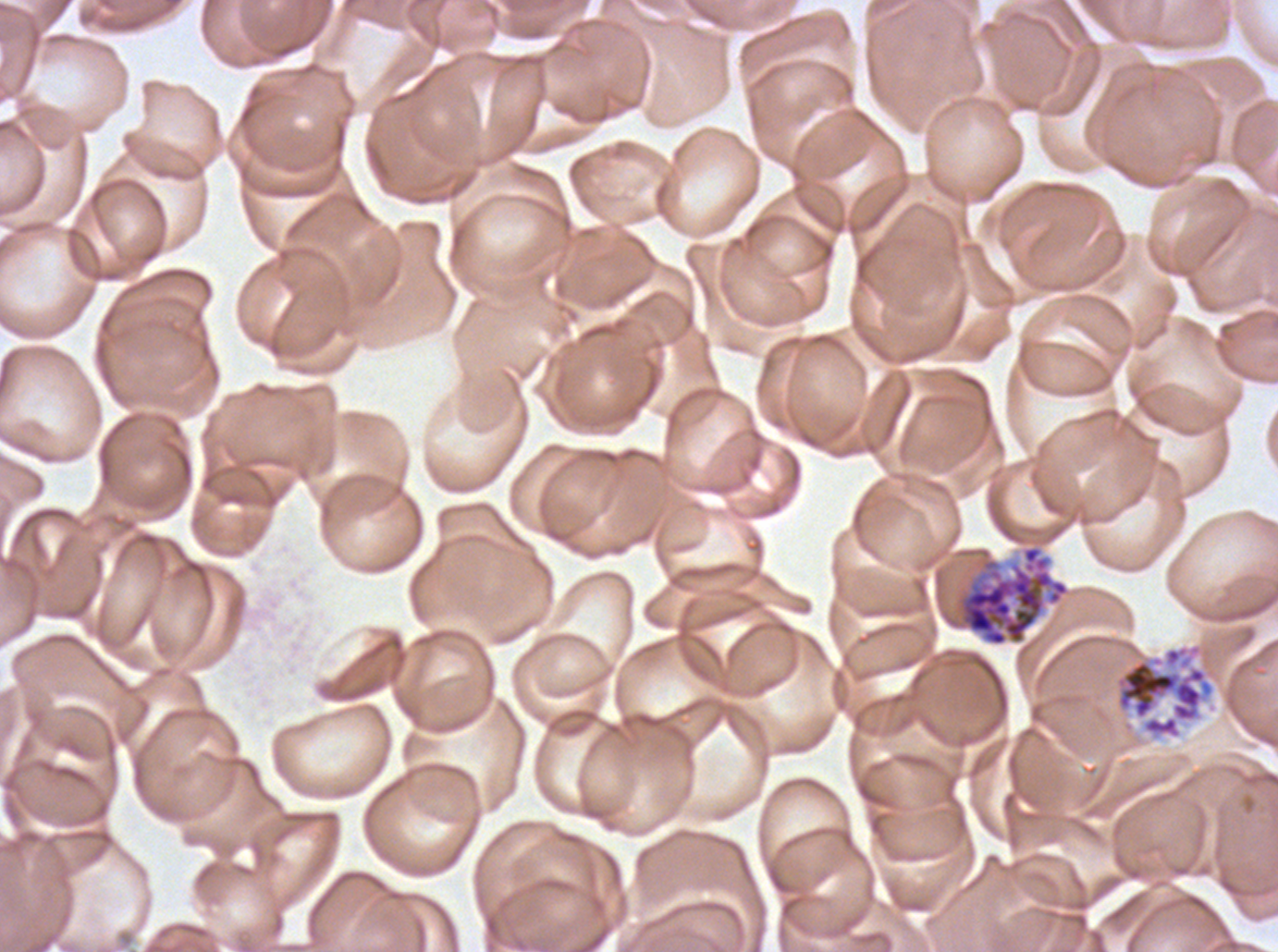

Approximate bounding rectangles given as corner coordinates in pixels from the top-left.
Summary:
  - Segmenter locations: (x1=945, y1=544, x2=1070, y2=647), (x1=1113, y1=642, x2=1215, y2=740)
  - Preparation: thin blood smear
  - Image size: 1278×952 pixels
  - Stain: Giemsa
  - Specimen: ex-vivo P. falciparum culture from a patient in The Gambia, grown for 24 to 48 hours
  - Field of view: sub-image separated from a larger composite